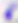
modality: photomicrograph
magnification: 400x
identification: Toxoplasma gondii